State which parasite is depicted.
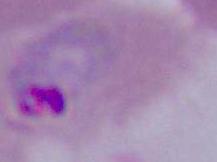

This is Plasmodium.

modality = micrograph
magnification = 400x or 1000x